Identify the parasite.
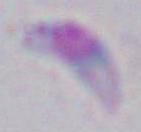
Toxoplasma gondii.

Photomicrograph. Captured at 1000x magnification.